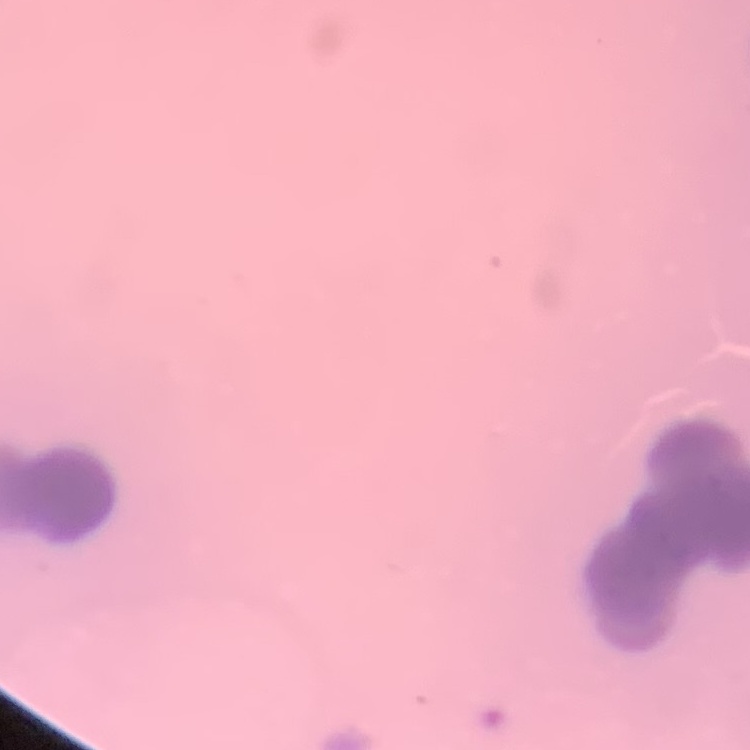

erythrocyte morphology = rouleaux formation
stain = Field's or Giemsa
preparation = thin peripheral smear
image type = one tile cut from a larger photomicrograph